Describe the morphology of the erythrocytes.
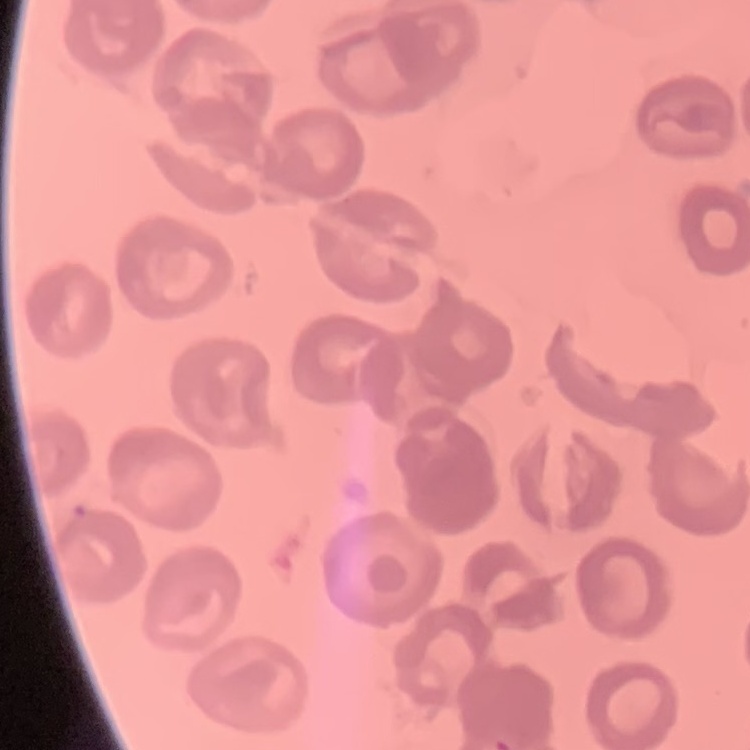

No rouleaux formation.

image type = one tile cut from a larger photomicrograph
preparation = thin blood smear
stain = Field's or Giemsa